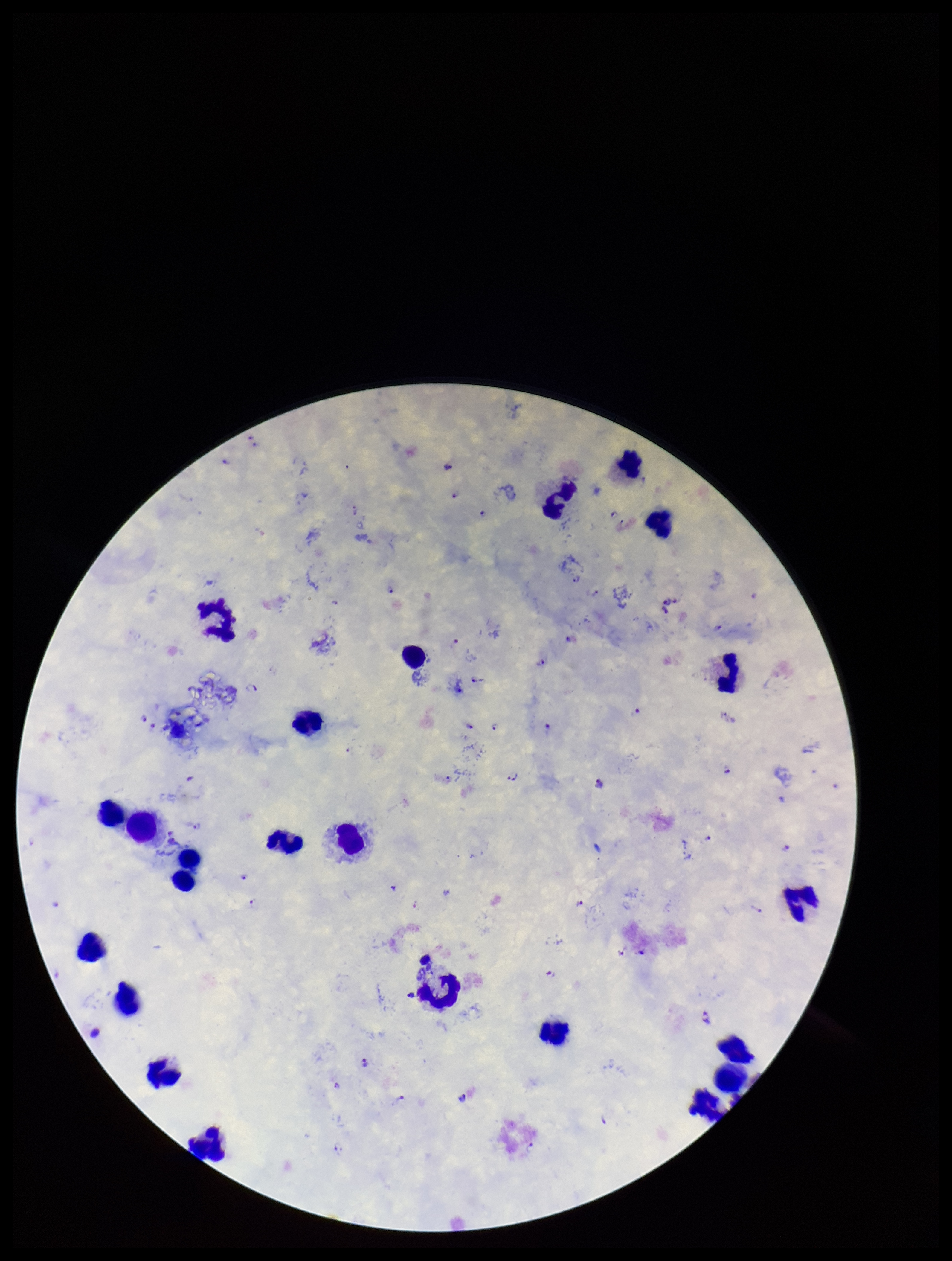 Image is 952×1261 pixels. Species reported for this patient: Plasmodium falciparum. Parasite count: 40. Giemsa stain. Single field of view. Patient malaria status: infected. Preparation: thick blood smear. Plasmodium parasites: seen. Smartphone photograph taken through the eyepiece of a microscope. Leukocyte count: 21.